Classify this cell by malaria status.
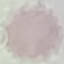
It is uninfected.

Acquired by smartphone through the microscope eyepiece. Automatically extracted cell patch, resized to 64 × 64 pixels. Giemsa-stained preparation. Thin blood smear.